Assess the morphology of the erythrocytes.
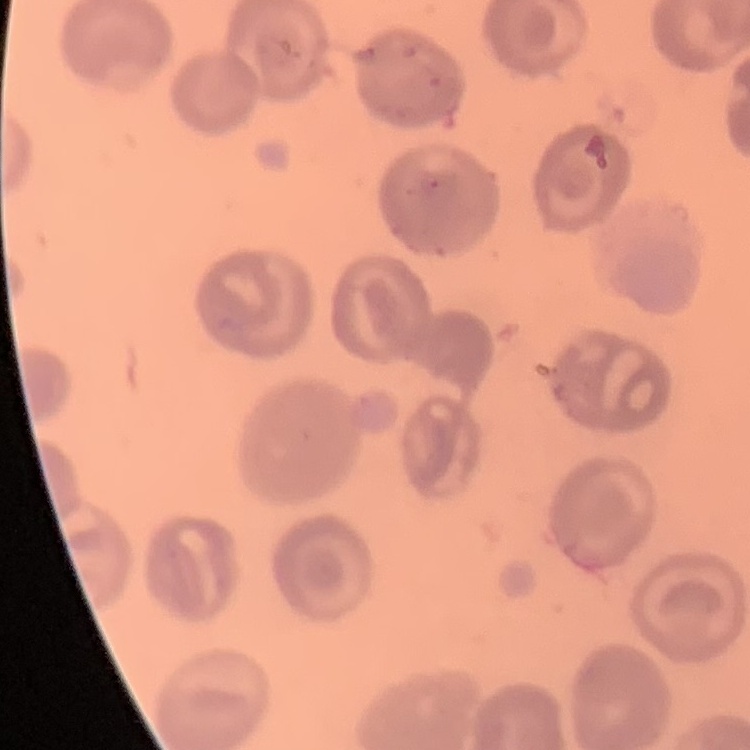
They show no rouleaux formation.

Summary:
  - Stain: Field's or Giemsa
  - Preparation: thin peripheral smear
  - Image type: one tile cut from a larger photomicrograph